Assess this cell for malaria.
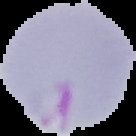

It is parasitized.

From a thin blood film. The area outside the segmented cell region is set to black. Image is 136×136 pixels.